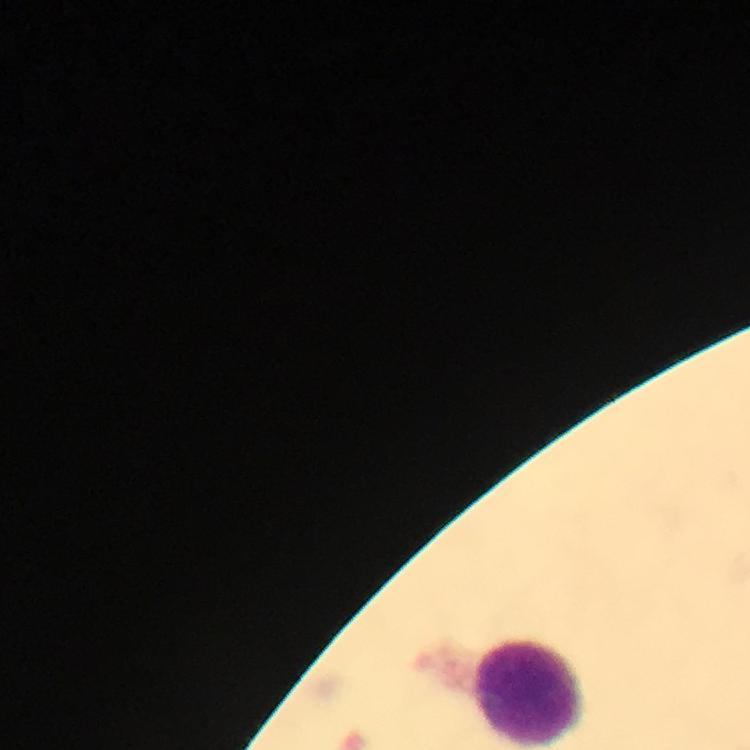 Approximate centers as (x, y) in pixels. Leukocyte locations: (529, 694). 100x magnification. Image is 750×750 pixels. Thick blood film. Plasmodium parasites: none detected. Photographed through the microscope with a smartphone camera. Immersion oil applied. A crop from one field of view. Giemsa stain. From a malaria diagnostic workup.